Name the parasite shown.
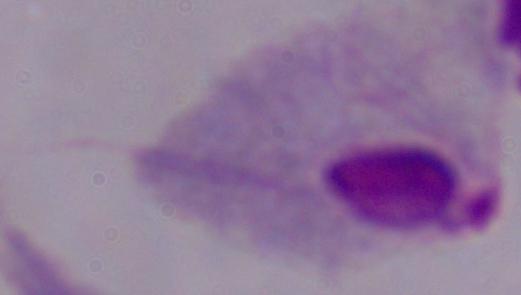

This is a trichomonad.

Micrograph. 1000x magnification.